Give the position of every Plasmodium parasite and every leukocyte.
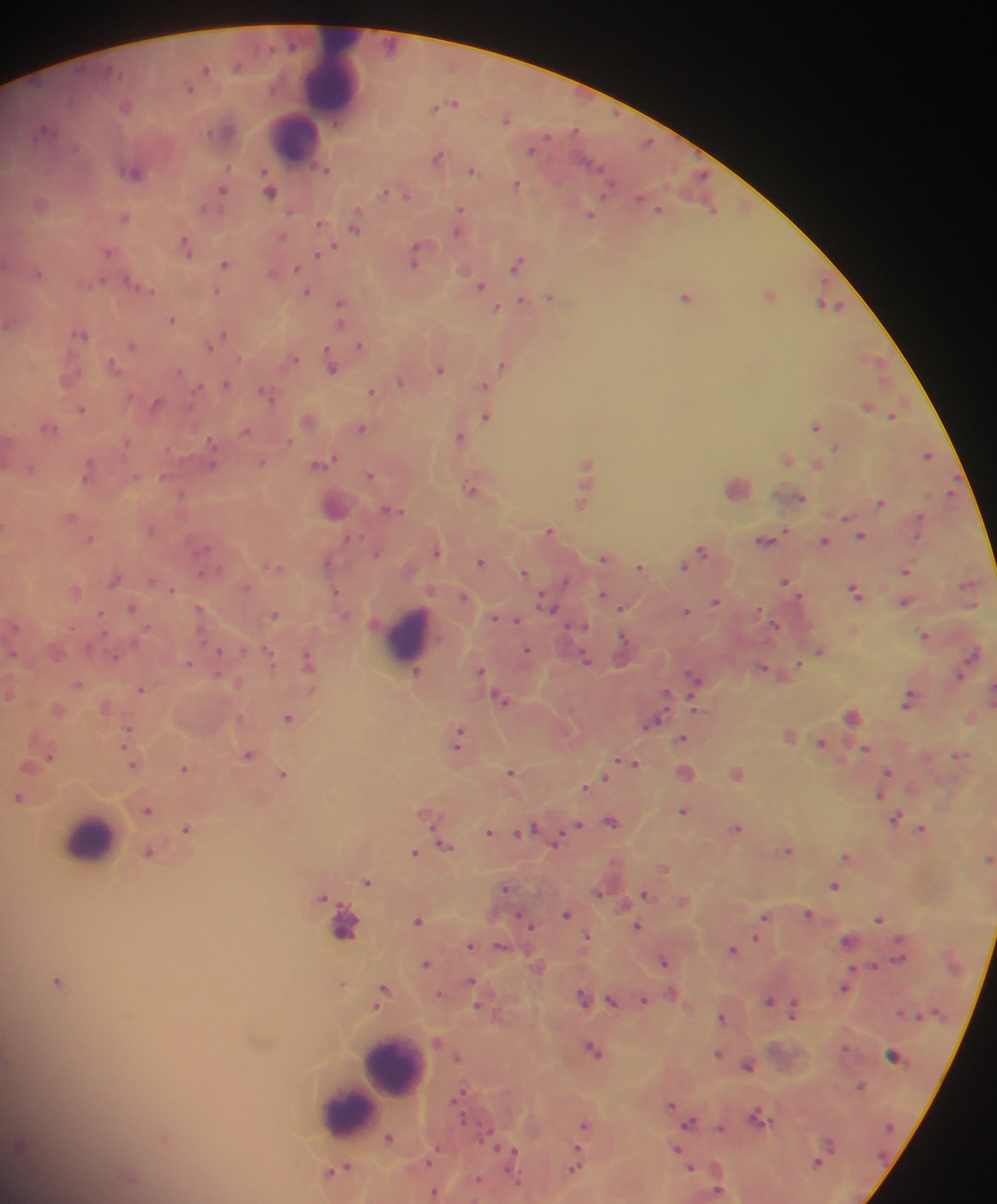
Approximate centers as [x, y] in pixels.
Plasmodium parasites: [206, 70], [191, 87], [453, 102], [126, 106], [507, 118], [45, 130], [532, 149], [438, 156], [327, 169], [472, 170], [135, 172], [517, 184], [270, 190], [221, 193], [389, 193], [403, 194], [41, 203], [658, 208], [712, 208], [461, 211], [591, 213], [125, 215], [356, 223], [322, 224], [460, 226], [187, 245], [110, 251], [319, 254], [417, 256], [226, 262], [518, 263], [298, 268], [37, 272], [141, 285], [481, 285], [218, 290], [306, 291], [770, 293], [551, 296], [686, 296], [522, 301], [831, 304], [497, 307], [341, 308], [172, 319], [81, 333], [222, 336], [216, 340], [210, 344], [133, 345], [360, 345], [294, 358], [876, 358], [332, 364], [504, 364], [115, 366], [440, 369], [401, 380], [226, 384], [485, 384], [372, 391], [268, 392], [157, 403], [869, 405], [82, 408], [894, 414], [487, 415], [308, 419], [816, 425], [49, 427], [362, 428], [246, 431], [461, 436], [838, 446], [928, 454], [788, 458], [261, 463], [588, 463], [322, 464], [819, 465], [89, 470], [371, 475], [738, 486], [473, 489], [951, 492], [795, 495], [881, 502], [583, 503], [335, 506], [394, 510], [72, 516], [847, 516], [920, 518], [550, 531], [861, 535], [91, 539], [767, 540], [825, 541], [702, 549], [438, 550], [604, 557], [329, 561], [482, 561], [685, 564], [275, 566], [641, 567], [905, 571], [525, 572], [116, 579], [566, 581], [786, 581], [247, 587], [171, 588], [76, 589], [857, 591], [336, 592], [603, 595], [464, 596], [716, 600], [905, 601], [547, 605], [133, 607], [623, 607], [201, 610], [687, 611], [276, 614], [496, 617], [506, 617], [515, 619], [774, 625], [926, 634], [528, 650], [821, 650], [220, 651], [269, 654], [309, 659], [587, 659], [189, 664], [799, 665], [482, 670], [772, 671], [416, 673], [960, 674], [695, 680], [79, 683], [141, 687], [992, 688], [502, 699], [910, 699], [106, 706], [58, 709], [854, 716], [289, 718], [651, 722], [128, 731], [791, 734], [460, 738], [684, 738], [823, 743], [866, 748], [250, 754], [961, 754], [629, 762], [133, 763], [185, 768], [889, 771], [512, 772], [685, 773], [737, 773], [283, 774], [605, 777], [586, 785], [882, 794], [20, 797], [148, 810], [685, 810], [429, 813], [897, 818], [612, 821], [579, 824], [737, 827], [187, 828], [923, 828], [525, 830], [491, 832], [557, 841], [444, 844], [426, 849], [788, 849], [149, 853], [416, 853], [847, 855], [989, 859], [664, 867], [367, 881], [835, 884], [506, 887], [599, 892], [647, 894], [325, 897], [684, 899], [568, 913], [809, 913], [765, 916], [525, 918], [880, 918], [419, 920], [638, 925], [758, 936], [588, 937], [849, 941], [471, 944], [502, 946], [734, 949], [899, 958], [666, 961], [427, 963], [539, 965], [874, 965], [59, 981], [473, 982], [845, 987], [383, 992], [439, 995], [584, 997], [644, 1000], [613, 1001], [770, 1001], [483, 1006], [794, 1007], [723, 1017], [594, 1049], [720, 1054], [893, 1056], [457, 1057], [749, 1065], [861, 1086], [461, 1095], [673, 1105], [760, 1117], [691, 1122], [585, 1124], [721, 1128], [165, 1137], [391, 1138], [677, 1149], [512, 1152], [431, 1158], [818, 1162], [576, 1166], [340, 1168], [691, 1169], [131, 1178], [479, 1180], [435, 1191], [718, 1192].
Leukocytes: [333, 77], [294, 139], [409, 634], [86, 838], [355, 936], [395, 1068], [377, 1091], [348, 1110].

Summary:
  - Country: Ghana
  - Image size: 997×1204 pixels
  - Field of view: single
  - Preparation: thick blood film
  - Capture: mobile-phone photograph through a microscope